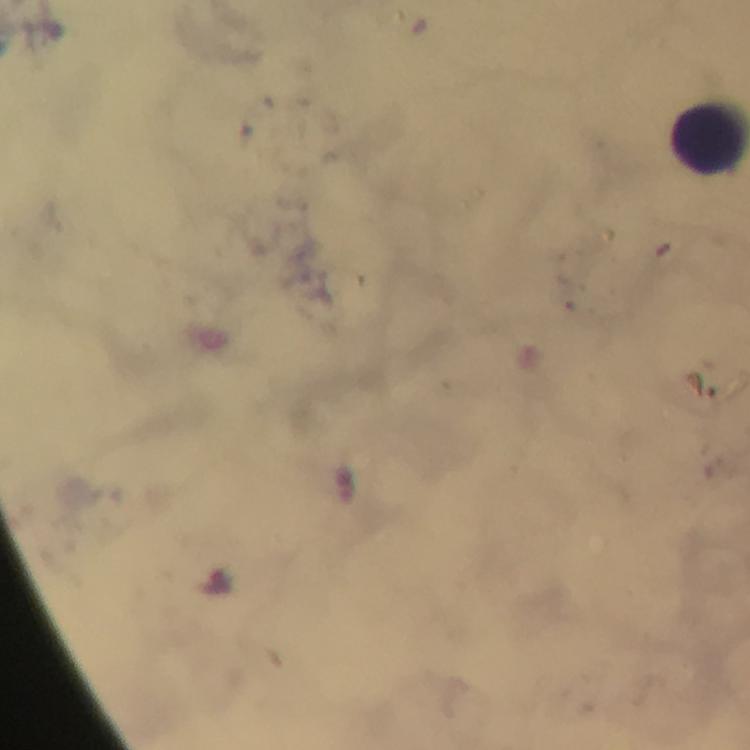

Approximate object centers, in pixels from the top-left corner. Malaria parasite locations: (x=214, y=582). Leukocyte locations: (x=708, y=140). Image is 750×750 pixels. Giemsa-stained preparation. Photographed through the microscope with a smartphone camera. Immersion oil applied. From a diagnostic examination for malaria. 100x magnification. Cropped region of a single field of view. Thick blood smear.